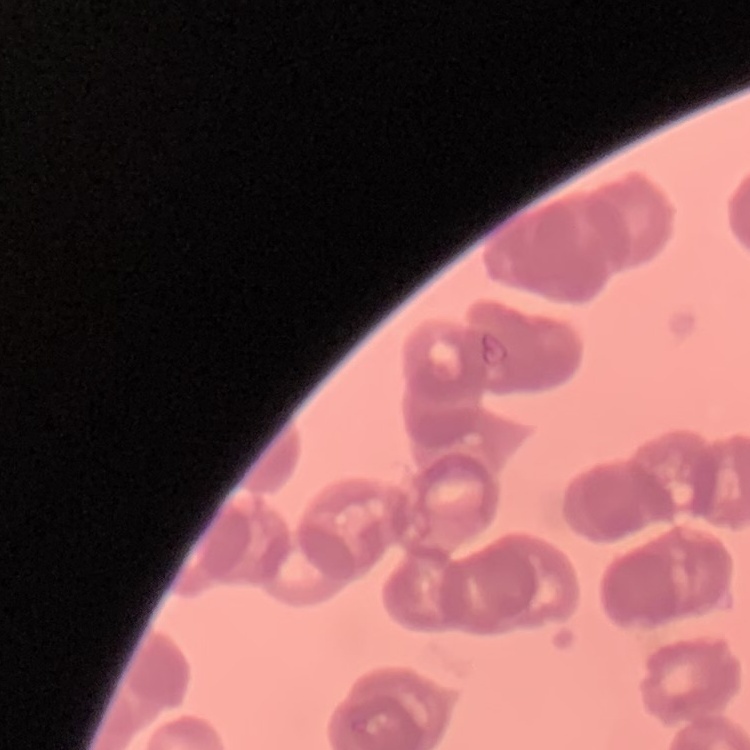

{
  "erythrocyte_morphology": "rouleaux formation",
  "image_type": "square crop of a larger photomicrograph",
  "preparation": "thin blood smear",
  "stain": "Field's or Giemsa"
}